Classify this cell by malaria status.
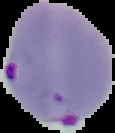

Parasitized.

Summary:
  - Preparation: thin blood film
  - Image size: 115×133 pixels
  - Image type: segmented cell region with the area outside set to black